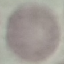

Result: no malaria parasites seen. Photographed with a smartphone camera at the microscope eyepiece. Giemsa stain. Automatically extracted cell patch, resized to 64 × 64 pixels. Thin blood smear.